Classify this cell by malaria status.
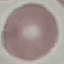

Uninfected.

preparation = thin smear
image type = cell patch, automatically extracted from a larger field of view and resized to 64 × 64 pixels
capture = smartphone camera at the microscope eyepiece
stain = Giemsa